Name the cell type shown.
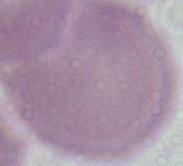
This is an erythrocyte.

magnification: 1000x
modality: photomicrograph